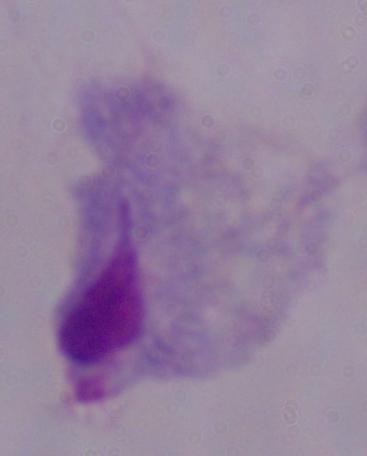
Summary:
  - Identification: trichomonad
  - Magnification: 1000x
  - Modality: micrograph